Identify the blood parasite species.
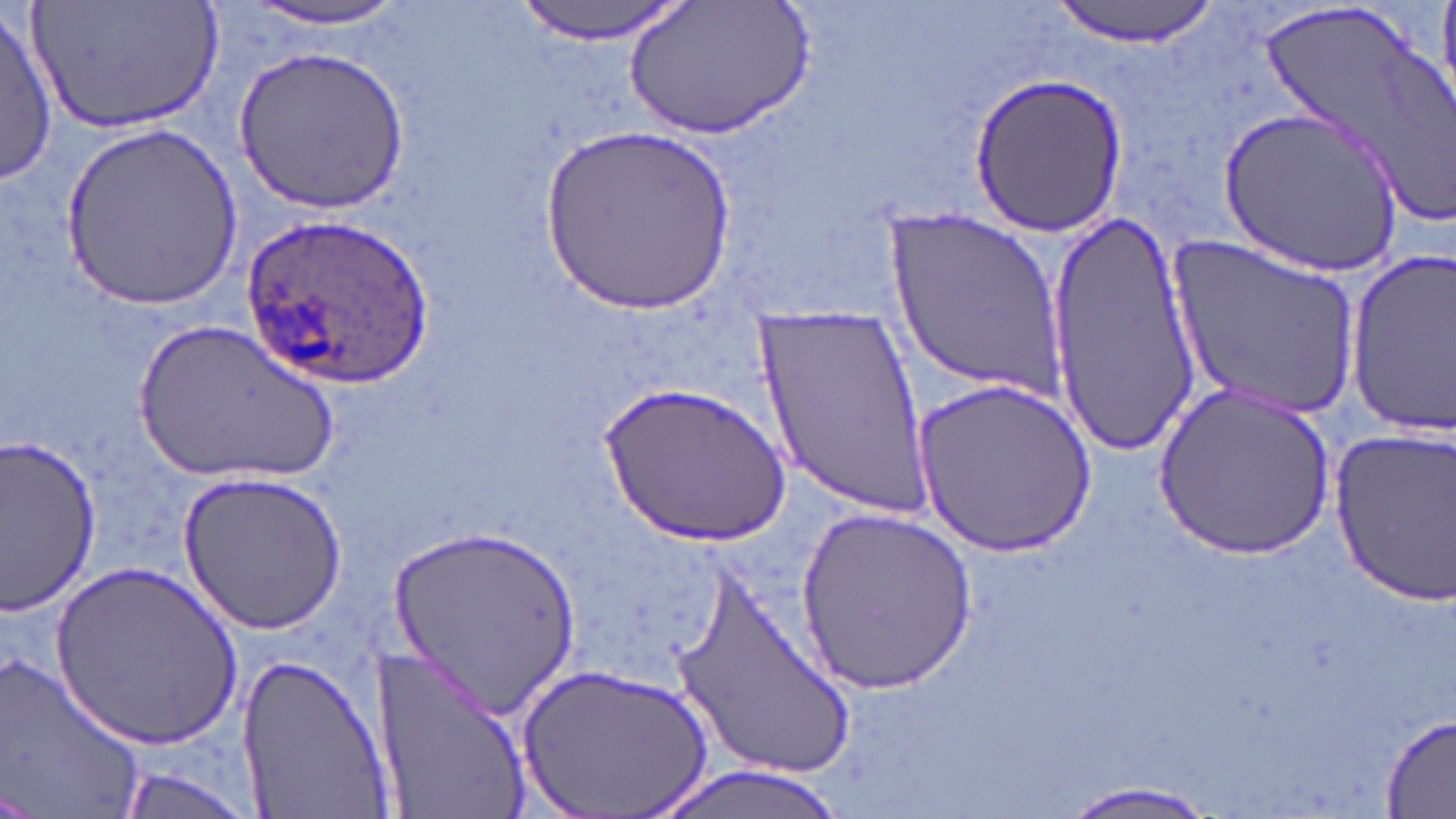
Plasmodium ovale.

Approximate bounding boxes as [x1, y1, x2, y2] in pixels. Uninfected red blood cell locations: [29, 0, 230, 135], [230, 0, 425, 33], [514, 0, 692, 42], [625, 0, 808, 140], [1050, 0, 1225, 45], [1261, 0, 1454, 229], [0, 12, 57, 184], [230, 45, 408, 213], [964, 72, 1131, 240], [1219, 103, 1406, 278], [63, 121, 241, 308], [543, 122, 737, 317], [886, 210, 1069, 395], [1045, 214, 1207, 459], [1168, 232, 1361, 422], [1344, 244, 1454, 437], [756, 308, 931, 517], [135, 320, 339, 486], [603, 378, 790, 550], [915, 378, 1096, 557], [1156, 382, 1339, 558], [1326, 424, 1456, 605], [0, 432, 103, 619], [181, 469, 346, 632], [795, 505, 975, 694], [388, 523, 581, 716], [51, 556, 242, 751], [675, 575, 858, 793], [377, 638, 532, 814], [0, 649, 149, 819], [235, 651, 391, 819], [514, 662, 717, 819], [1379, 712, 1456, 819], [115, 763, 260, 819], [647, 763, 857, 819], [1052, 777, 1223, 819]. Plasmodium ovale-infected red blood cell locations: [246, 215, 433, 386]. Single field of view. May-Grünwald-Giemsa stain. Light microscopy. Image is 1456×819 pixels. Thin blood smear. Captured at 1000x magnification.